Describe the morphology of the erythrocytes.
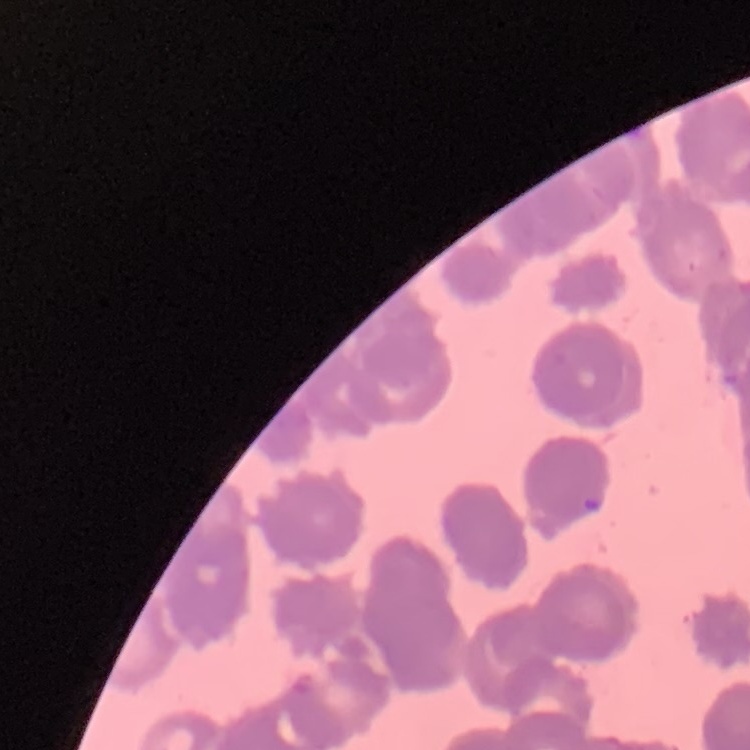
They show rouleaux formation.

Stained with either Field's or Giemsa. Thin blood smear. Square crop of a larger photomicrograph.